Describe the morphology of the red blood cells.
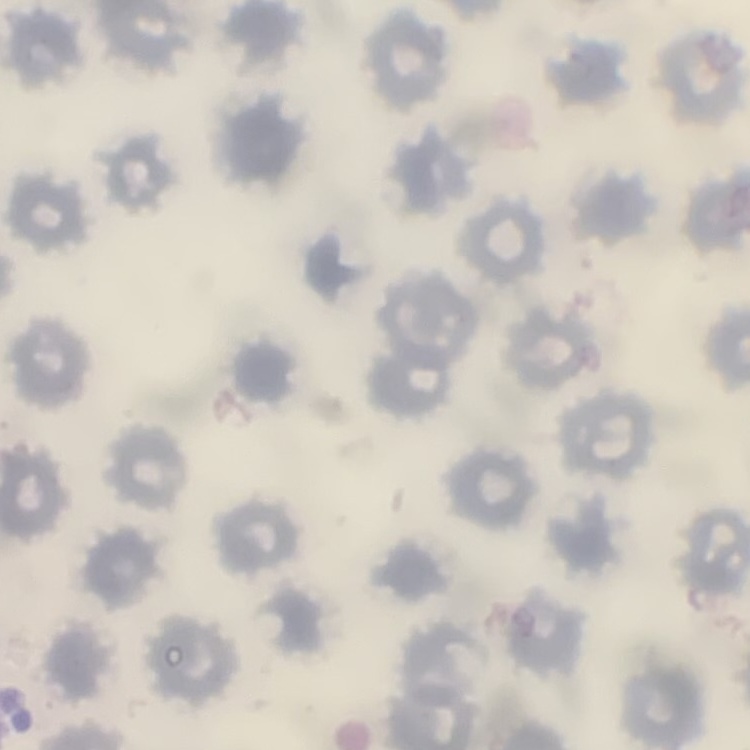
They show no rouleaux formation.

Summary:
  - Image type: one tile cut from a larger photomicrograph
  - Preparation: thin peripheral smear
  - Stain: Field's or Giemsa